State which parasite is depicted.
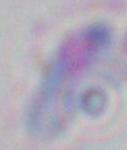

This is Toxoplasma gondii.

Summary:
  - Magnification: 1000x
  - Modality: micrograph